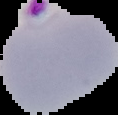 Malaria status: parasitized. From a thin blood film. Cell region segmented out of the field of view; the surrounding area is masked to black. Image is 118×115 pixels.